Assess the morphology of the erythrocytes.
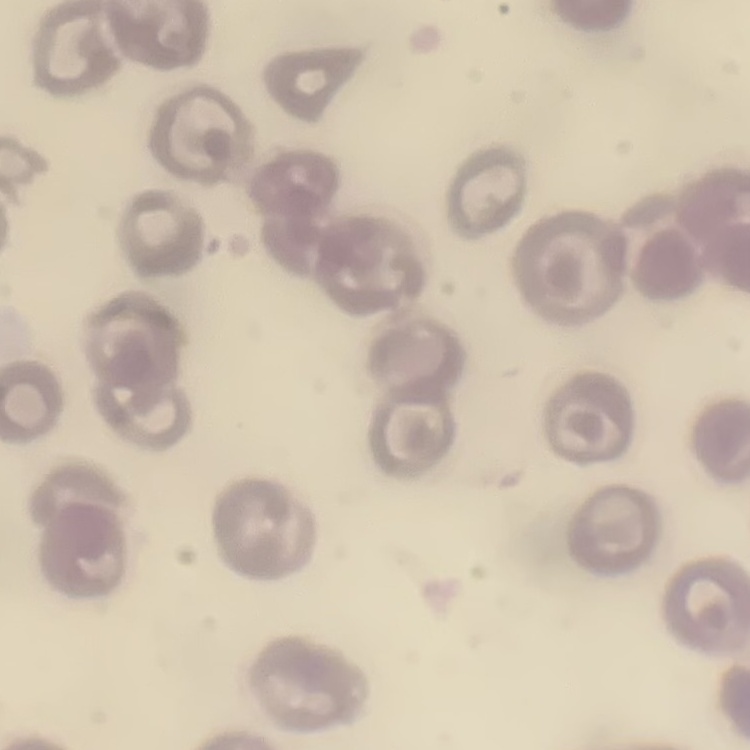
No rouleaux formation.

stain = Field's or Giemsa
image type = square crop of a larger photomicrograph
preparation = thin blood film